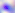
Photomicrograph. Toxoplasma gondii is seen. 400x magnification.